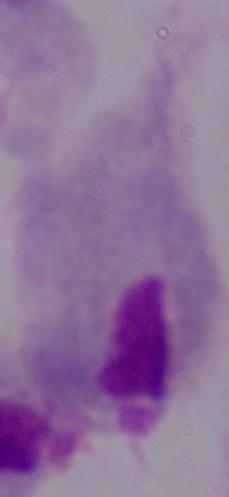
Summary:
  - Identification: trichomonad
  - Magnification: 1000x
  - Modality: micrograph